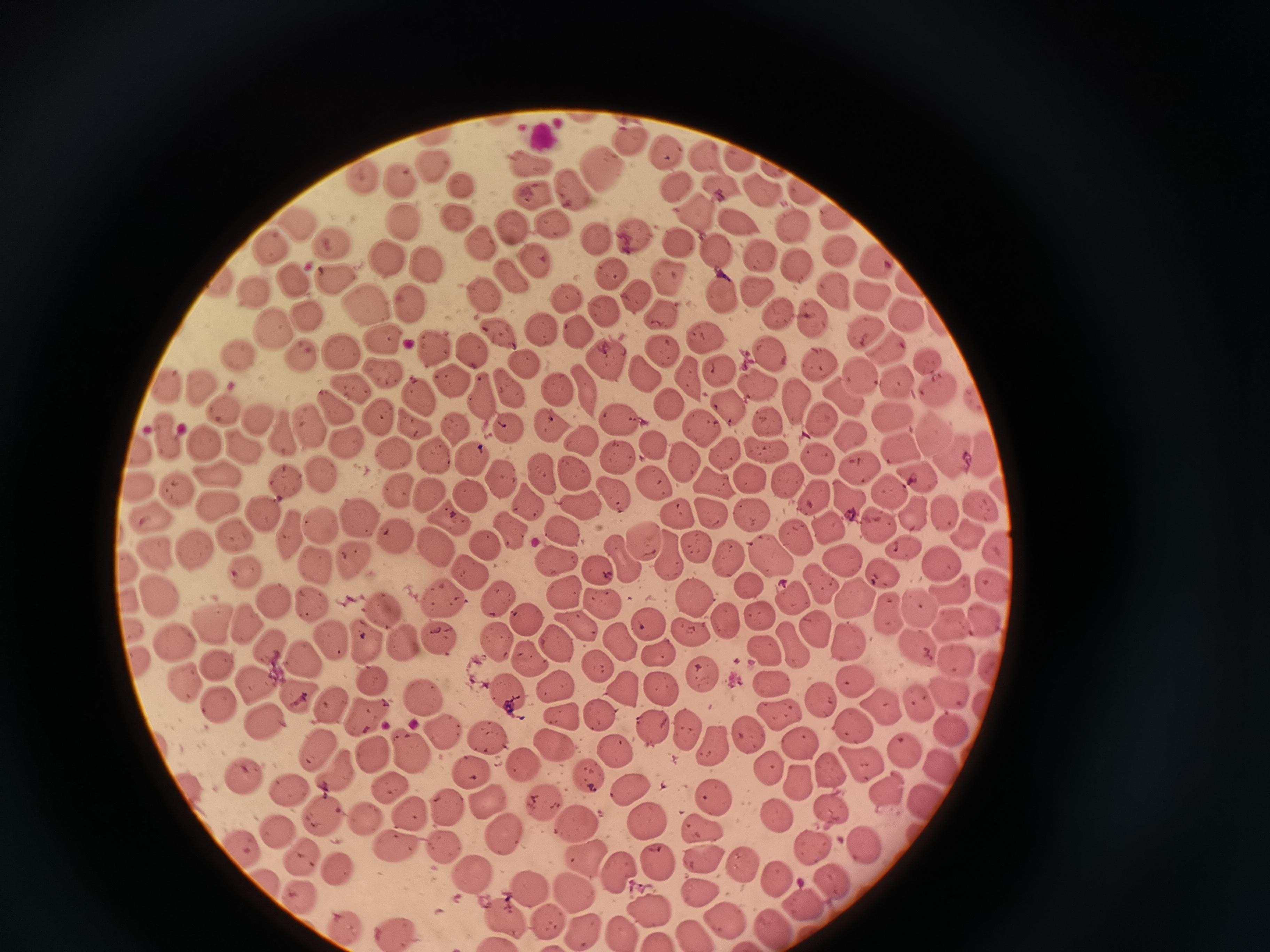

Approximate centers as (x, y) in pixels. Cell locations: (630, 138), (666, 151), (700, 154), (736, 159), (435, 163), (526, 163), (605, 170), (401, 180), (461, 184), (670, 185), (573, 187), (721, 187), (762, 191), (798, 191), (533, 198), (835, 216), (298, 218), (694, 218), (457, 220), (405, 221), (794, 225), (511, 228), (739, 228), (554, 229), (597, 237), (637, 237), (680, 241), (334, 242), (272, 243), (477, 246), (716, 250), (387, 255), (837, 255), (766, 259), (876, 259), (532, 260), (425, 263), (801, 263), (611, 269), (670, 277), (336, 278), (509, 279), (293, 281), (904, 283), (222, 284), (725, 290), (760, 290), (831, 291), (479, 293), (635, 294), (871, 294), (255, 295), (566, 299), (371, 305), (412, 305), (605, 311), (308, 312), (664, 314), (776, 315), (904, 315), (816, 319), (272, 328), (864, 328), (499, 333), (541, 333), (579, 334), (704, 335), (381, 343), (436, 347), (662, 348), (888, 349), (468, 351), (340, 352), (240, 355), (771, 357), (603, 360), (302, 361), (926, 361), (816, 362), (523, 366), (718, 368), (384, 373), (646, 373), (685, 373), (859, 374), (452, 376), (897, 380), (581, 384), (756, 384), (197, 386), (508, 386), (167, 387), (351, 388), (936, 389), (555, 390), (425, 396), (480, 396), (844, 396), (796, 399), (331, 407), (673, 407), (726, 408), (222, 409), (891, 412), (258, 416), (617, 417), (769, 419), (375, 420), (820, 420), (410, 424), (508, 425), (549, 425), (697, 426), (306, 428), (452, 428), (281, 432), (850, 433), (934, 434), (165, 437), (202, 440), (585, 440), (654, 443), (346, 444), (766, 446), (242, 447), (897, 449), (141, 451), (399, 451), (436, 452), (721, 452), (820, 457), (981, 457), (678, 458), (469, 459), (622, 460), (860, 469), (574, 472), (214, 474), (786, 474), (915, 474), (320, 475), (544, 475), (501, 476), (284, 480), (749, 481), (715, 482), (138, 487), (656, 488), (612, 489), (891, 490), (399, 491), (425, 492), (465, 492), (180, 494), (812, 494), (849, 496), (525, 500), (977, 500), (217, 502), (578, 505), (262, 510), (941, 510), (710, 512), (913, 513), (357, 515), (754, 515), (678, 517), (447, 520), (827, 522), (876, 522), (321, 524), (152, 526), (508, 528), (558, 529), (291, 531), (792, 533), (968, 533), (393, 534), (234, 535), (644, 543), (697, 545), (486, 546), (437, 547), (665, 549), (726, 549), (1000, 549), (904, 550), (198, 552), (620, 557), (770, 557), (156, 558), (351, 559), (557, 560), (839, 562), (941, 562), (132, 565), (595, 565), (319, 568), (876, 569), (469, 572), (246, 575), (817, 584), (990, 584), (749, 588), (568, 591), (790, 592), (158, 593), (953, 593), (440, 596), (308, 598), (690, 598), (276, 599), (497, 600), (130, 602), (856, 602), (604, 606), (378, 607), (920, 610), (887, 611), (758, 613), (525, 619), (988, 621), (645, 622), (726, 623), (243, 625), (949, 626), (216, 627), (571, 627), (817, 627), (135, 630), (690, 631), (175, 638), (333, 638), (850, 639), (367, 641), (442, 641), (614, 641), (406, 644), (500, 645), (275, 648), (554, 648), (917, 648), (794, 649), (760, 653), (660, 656), (523, 658), (310, 660), (137, 661), (219, 661), (600, 664), (955, 670), (991, 671), (707, 673), (858, 678), (368, 680), (181, 681), (767, 682), (252, 686), (622, 686), (662, 689), (299, 692), (557, 692), (945, 692), (507, 694), (825, 695), (426, 699), (216, 701), (988, 702), (327, 705), (917, 705), (880, 708), (362, 713), (557, 714), (596, 715), (780, 715), (854, 720), (264, 725), (436, 730), (958, 731), (658, 733), (686, 733), (750, 735), (484, 739), (556, 742), (803, 742), (316, 749), (613, 751), (710, 751), (375, 752), (903, 753), (411, 754), (525, 764), (862, 765), (944, 765), (470, 769), (829, 769), (586, 773), (765, 774), (244, 777), (336, 779), (799, 781), (387, 785), (195, 790), (287, 790), (627, 791), (890, 792), (714, 795), (489, 798), (925, 799), (446, 802), (542, 804), (832, 807), (408, 812), (779, 817), (322, 818), (361, 818), (575, 819), (704, 823), (507, 828), (277, 829), (647, 829), (445, 842), (389, 844), (816, 849), (869, 851), (706, 852), (246, 853), (587, 854), (303, 857), (741, 862), (657, 863), (333, 867), (617, 867), (471, 872), (775, 878), (269, 882), (529, 883), (834, 886), (699, 890), (575, 894), (303, 895), (800, 904), (649, 910), (509, 915), (552, 918), (723, 919), (768, 929), (395, 930), (346, 931), (585, 931), (620, 931). One field from this slide. Acquired by smartphone through the microscope eyepiece. Thin smear of blood. Giemsa-stained preparation. Image is 1270×952 pixels.